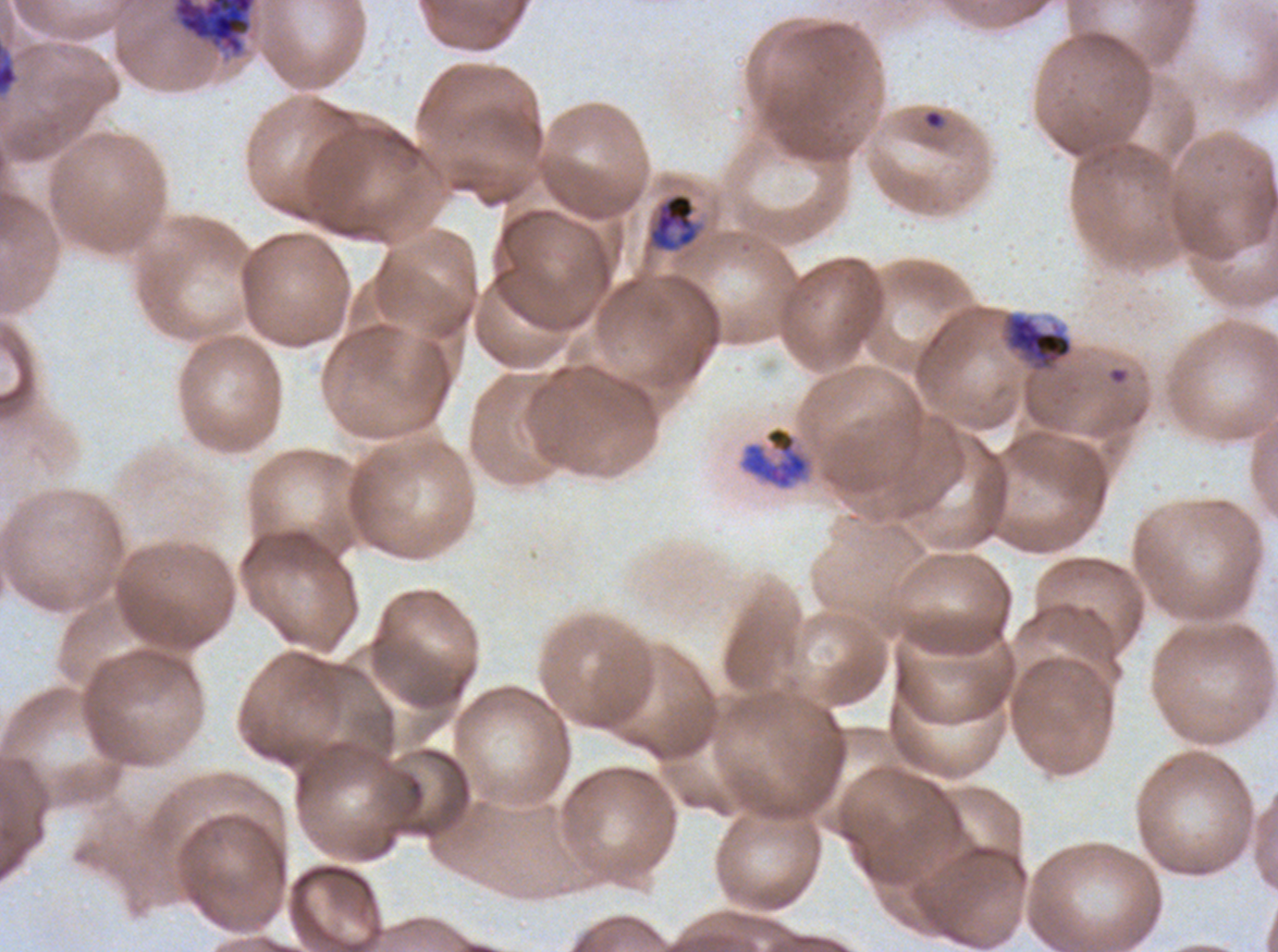
Approximate bounding boxes as (x1, y1, x2, y2) in pixels.
Summary:
  - Mid trophozoite locations: (648, 192, 699, 252)
  - Late trophozoite locations: (1006, 314, 1073, 369), (737, 425, 816, 492)
  - Ring locations: (925, 110, 943, 128)
  - Early schizont locations: (0, 43, 18, 96)
  - Late schizont locations: (171, 0, 257, 57)
  - Field of view: one sub-image of a larger composite
  - Specimen: P. falciparum from a patient in The Gambia, cultured ex vivo for 24 to 48 hours
  - Preparation: thin blood film
  - Life-cycle stages observed: ring, mid trophozoite, late trophozoite, early schizont, late schizont
  - Stain: Giemsa
  - Image size: 1278×952 pixels